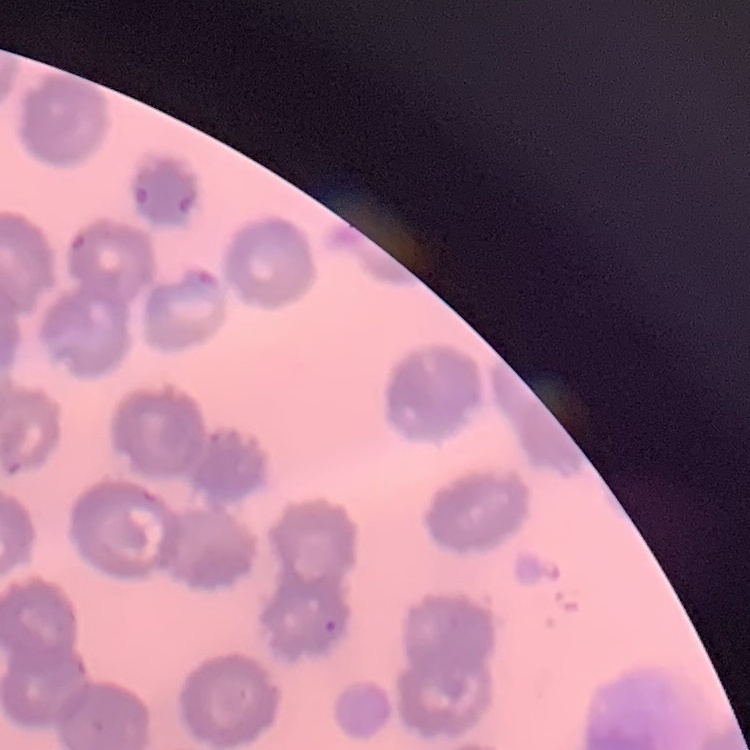 The erythrocytes exhibit no rouleaux formation. Field's or Giemsa stain. Square crop of a larger photomicrograph. Thin blood film.